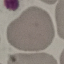 Malaria status: uninfected. Cell patch, automatically extracted from a larger field of view and resized to 64 × 64 pixels. Thin blood smear. Giemsa-stained preparation. Photographed with a smartphone camera at the microscope eyepiece.